Comment on the morphology of the erythrocytes.
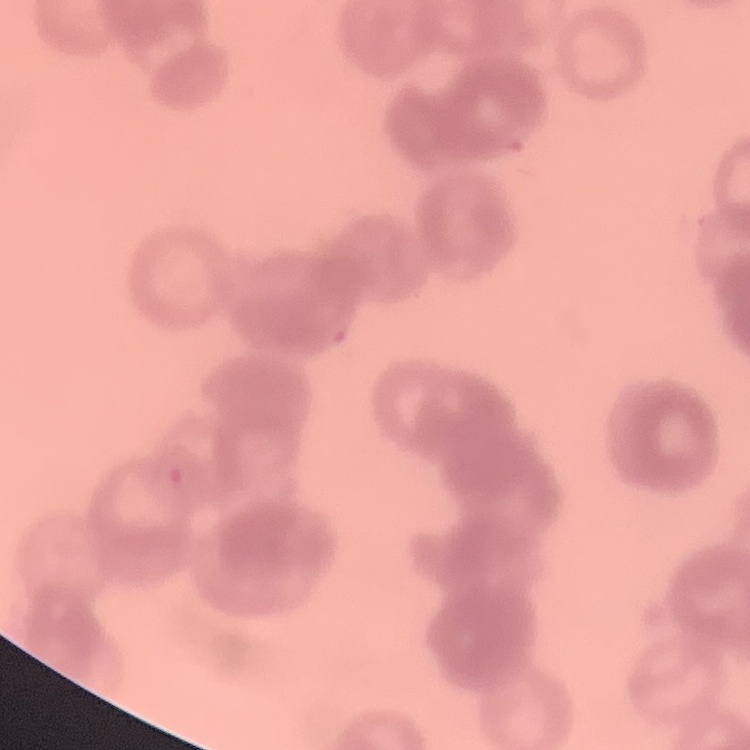

Rouleaux formation.

Square crop of a larger photomicrograph. Field's or Giemsa stain. Thin blood smear.